Comment on the morphology of the erythrocytes.
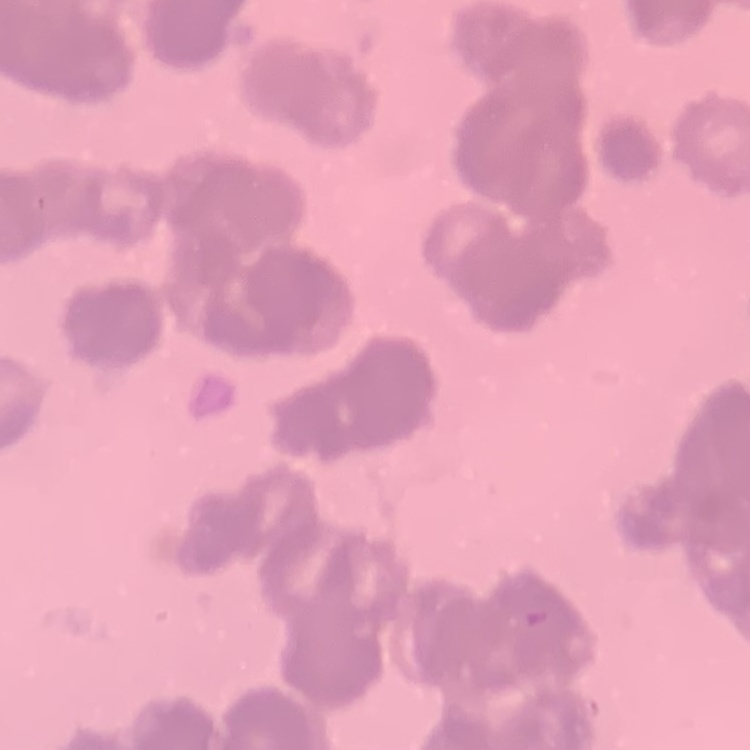
They show rouleaux formation.

{
  "stain": "Field's or Giemsa",
  "preparation": "thin blood smear",
  "image_type": "one tile cut from a larger photomicrograph"
}